Name the blood parasite species.
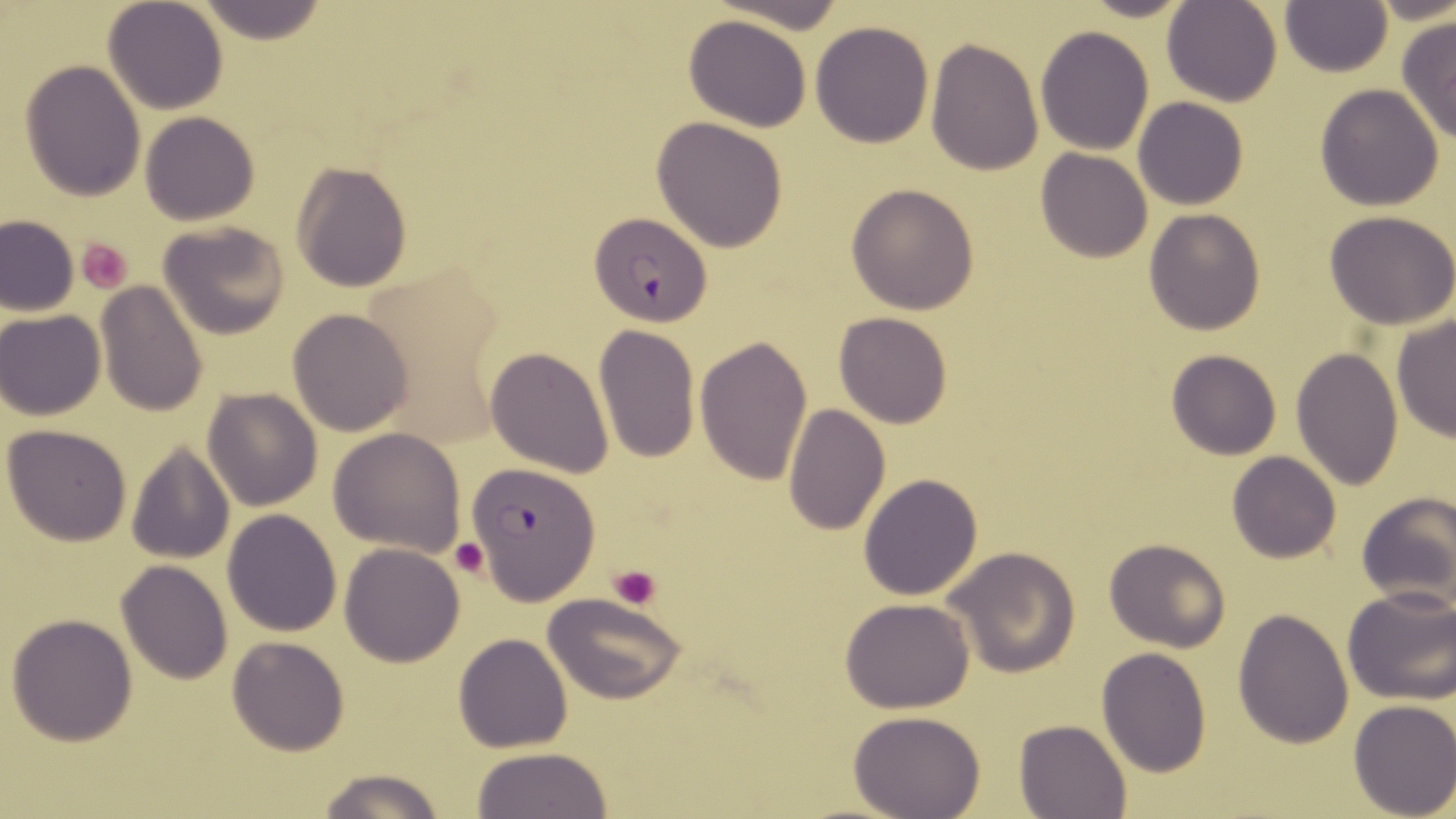
Plasmodium falciparum.

Summary:
  - Coordinate format: approximate bounding boxes as (x1, y1, x2, y2) in pixels
  - Platelet locations: (76, 237, 135, 292), (449, 538, 488, 577), (609, 562, 663, 609)
  - Plasmodium falciparum-infected red blood cell locations: (589, 214, 713, 324), (465, 461, 599, 603)
  - Uninfected red blood cell locations: (102, 0, 228, 114), (1076, 0, 1198, 22), (195, 1, 333, 46), (1161, 1, 1284, 106), (1280, 1, 1393, 77), (684, 15, 813, 131), (1396, 16, 1456, 145), (810, 20, 935, 148), (1036, 25, 1154, 155), (926, 37, 1043, 178), (19, 60, 146, 200), (1314, 84, 1445, 211), (1133, 97, 1247, 210), (139, 111, 260, 225), (650, 116, 789, 252), (1035, 148, 1154, 263), (290, 161, 413, 293), (845, 182, 980, 316), (1143, 208, 1267, 335), (1325, 210, 1456, 329), (0, 215, 79, 317), (158, 221, 292, 339), (97, 283, 208, 417), (287, 308, 413, 436), (1, 310, 105, 420), (832, 312, 956, 429), (1391, 312, 1456, 446), (592, 324, 701, 465), (696, 336, 813, 484), (485, 345, 614, 478), (1291, 346, 1403, 489), (1165, 349, 1283, 460), (201, 388, 324, 511), (784, 402, 890, 536), (3, 424, 132, 546), (329, 426, 465, 555), (125, 442, 235, 565), (1227, 450, 1342, 563), (858, 473, 983, 600), (1354, 492, 1456, 612), (222, 508, 343, 635), (1103, 536, 1231, 654), (339, 542, 466, 666), (943, 546, 1081, 678), (115, 562, 233, 684), (1342, 586, 1456, 705), (544, 594, 685, 704), (841, 599, 975, 713), (1232, 607, 1356, 748), (6, 612, 139, 745), (453, 633, 573, 753), (226, 636, 349, 756), (1096, 647, 1211, 777), (1347, 699, 1456, 819), (849, 711, 987, 819), (1015, 719, 1132, 818), (467, 747, 614, 819), (315, 766, 443, 819)
  - Preparation: thin blood film
  - Magnification: 1000x
  - Modality: optical microscopy
  - Image size: 1456×819 pixels
  - Field of view: single
  - Stain: May-Grünwald-Giemsa